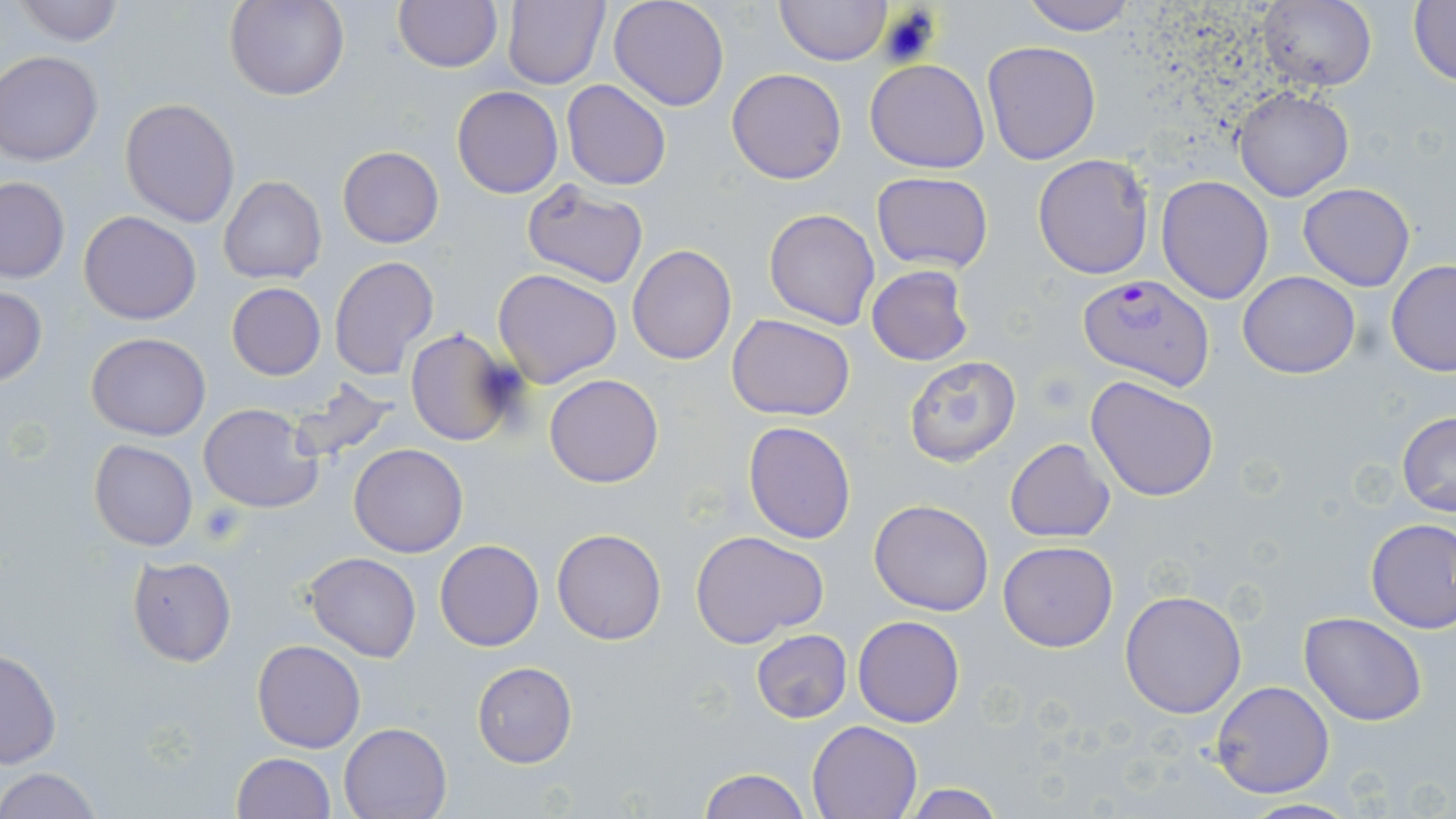
Summary:
  - Coordinate format: approximate bounding boxes as [x1, y1, x2, y2] in pixels
  - Plasmodium falciparum-infected red blood cell locations: [1078, 273, 1215, 389]
  - Uninfected red blood cell locations: [13, 0, 126, 46], [225, 0, 348, 102], [502, 0, 610, 91], [608, 0, 728, 110], [776, 0, 891, 66], [1020, 0, 1137, 36], [1259, 0, 1377, 93], [1408, 0, 1456, 87], [394, 1, 502, 72], [982, 41, 1102, 166], [1, 51, 103, 166], [865, 60, 989, 173], [726, 68, 848, 184], [562, 78, 671, 191], [451, 85, 563, 198], [1232, 87, 1355, 202], [119, 96, 240, 228], [337, 145, 444, 248], [1032, 154, 1154, 279], [869, 173, 994, 272], [1156, 175, 1273, 304], [219, 176, 326, 285], [0, 178, 71, 284], [520, 180, 650, 289], [1297, 182, 1415, 292], [764, 208, 880, 329], [79, 210, 202, 325], [627, 245, 738, 366], [329, 256, 439, 381], [1385, 259, 1456, 377], [865, 266, 974, 366], [492, 268, 621, 390], [1237, 271, 1360, 379], [226, 283, 327, 379], [0, 286, 48, 387], [727, 314, 855, 421], [403, 330, 523, 446], [85, 332, 211, 441], [903, 355, 1022, 466], [545, 374, 663, 488], [1086, 376, 1219, 502], [285, 379, 405, 464], [200, 404, 324, 513], [1396, 411, 1456, 518], [743, 420, 857, 544], [1005, 438, 1114, 542], [89, 439, 197, 551], [349, 443, 468, 557], [870, 500, 994, 615], [1365, 518, 1456, 634], [552, 528, 666, 646], [691, 530, 828, 647], [998, 539, 1118, 652], [435, 540, 544, 651], [304, 552, 422, 662], [127, 556, 236, 667], [1120, 590, 1248, 718], [1300, 611, 1428, 725], [853, 615, 964, 727], [751, 629, 852, 723], [251, 640, 366, 753], [0, 647, 61, 770], [471, 662, 577, 768], [1210, 680, 1336, 799], [806, 719, 923, 818], [338, 721, 453, 818], [231, 752, 335, 818], [695, 766, 812, 819], [0, 767, 102, 819], [901, 783, 1004, 819], [1238, 799, 1363, 818]
  - Platelet locations: [196, 500, 249, 547]
  - Slide-level diagnosis: Plasmodium falciparum
  - Stain: May-Grünwald-Giemsa
  - Preparation: thin blood film
  - Modality: optical microscopy
  - Field of view: single
  - Magnification: 1000x
  - Image size: 1456×819 pixels